Assess this cell for malaria.
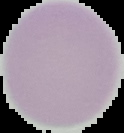
It is uninfected.

The area outside the segmented cell region is set to black. From a thin blood film. Image is 124×133 pixels.